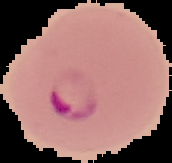
image size = 172×163 pixels
malaria status = parasitized
preparation = thin blood film
image type = segmented cell region on a black background